Outline each blood parasite and name the species.
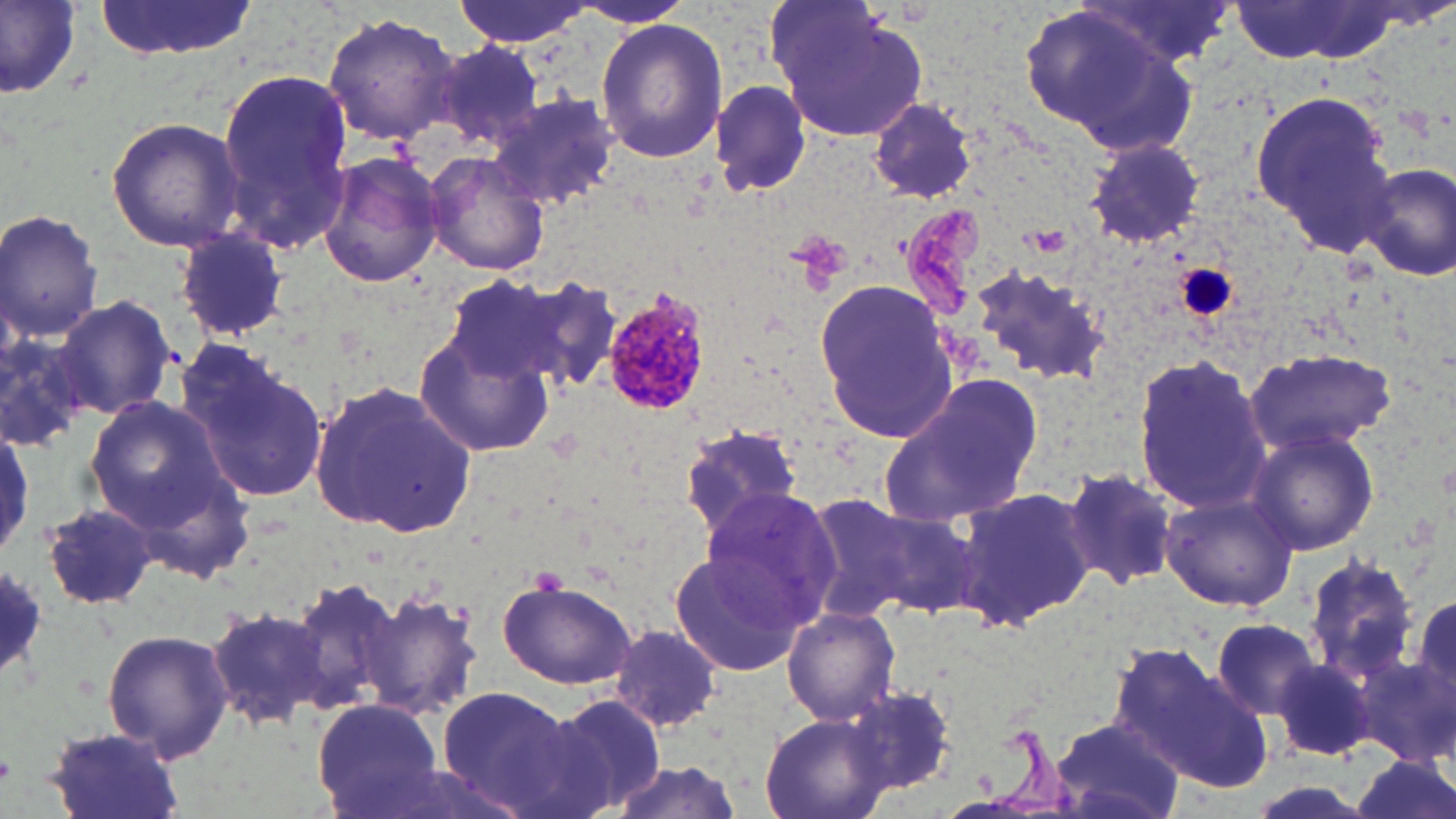

Approximate bounding boxes as (x1, y1, x2, y2) in pixels.
Plasmodium malariae-infected red blood cells: (601, 289, 712, 420).
No Plasmodium falciparum, Plasmodium ovale, Plasmodium vivax, Babesia divergens, or Trypanosoma brucei observed.

Platelet locations: (1175, 262, 1237, 321). Uninfected red blood cell locations: (94, 0, 259, 61), (452, 0, 589, 49), (574, 0, 693, 29), (1082, 0, 1236, 65), (2, 1, 82, 104), (1230, 1, 1410, 63), (769, 2, 929, 141), (1020, 3, 1193, 148), (322, 13, 459, 144), (595, 20, 728, 163), (431, 40, 541, 149), (218, 70, 357, 255), (710, 80, 812, 199), (1251, 91, 1393, 254), (491, 93, 622, 210), (867, 99, 979, 202), (106, 117, 244, 252), (1084, 138, 1207, 247), (316, 151, 446, 289), (423, 151, 551, 277), (1357, 162, 1456, 281), (0, 208, 105, 342), (173, 230, 292, 343), (964, 262, 1113, 386), (442, 276, 577, 383), (504, 276, 626, 399), (813, 278, 959, 445), (54, 296, 178, 420), (414, 328, 557, 457), (1, 332, 90, 451), (179, 341, 329, 507), (1241, 345, 1397, 457), (1132, 354, 1274, 518), (879, 376, 1040, 527), (308, 379, 478, 537), (84, 398, 229, 527), (0, 420, 34, 563), (676, 421, 808, 541), (1246, 427, 1379, 555), (1061, 467, 1180, 590), (953, 481, 1098, 631), (695, 488, 842, 632), (1158, 489, 1299, 610), (800, 495, 927, 624), (39, 504, 158, 613), (861, 504, 985, 620), (668, 547, 811, 680), (1299, 554, 1421, 683), (287, 575, 408, 721), (496, 577, 637, 689), (359, 588, 485, 723), (1409, 589, 1454, 719), (204, 603, 335, 728), (783, 606, 901, 727), (1210, 617, 1321, 720), (606, 622, 724, 732), (103, 627, 233, 763), (1111, 643, 1272, 794), (1274, 658, 1380, 763), (435, 685, 586, 815), (842, 685, 957, 797), (539, 692, 668, 818), (311, 698, 449, 817), (758, 713, 896, 819), (1050, 716, 1180, 819), (42, 726, 188, 819), (1346, 756, 1456, 819), (593, 760, 749, 819). Slide-level diagnosis: Plasmodium malariae. Optical microscopy. One field of a larger specimen. Image is 1456×819 pixels. 1000x magnification. May-Grünwald-Giemsa stain. Thin blood film.